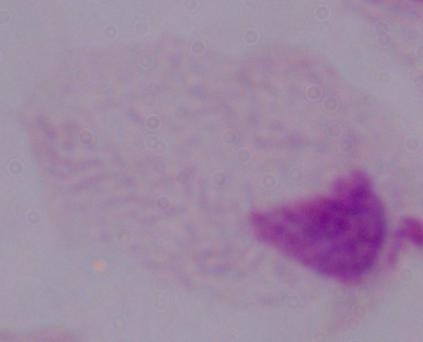

A trichomonad is shown. Captured at 1000x magnification. Micrograph.